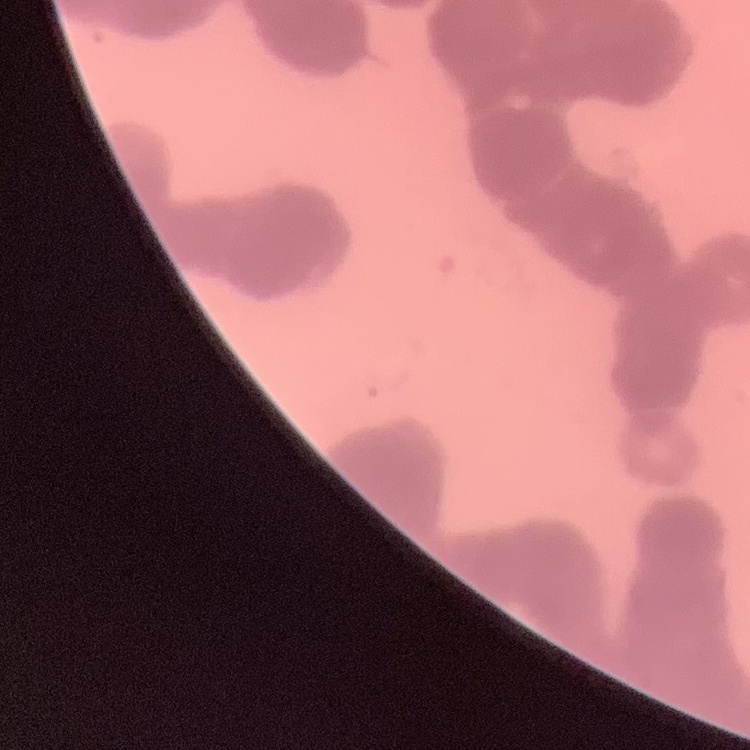
The red blood cells exhibit rouleaux formation. Field's or Giemsa stain. Thin blood film. Square crop of a larger photomicrograph.